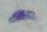

Micrograph. 1000x magnification. Toxoplasma gondii is shown.